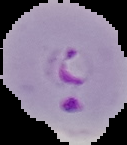

result = malaria parasites detected
image type = segmented cell region on a black background
preparation = thin blood film
image size = 127×145 pixels